Report the malaria status of this cell.
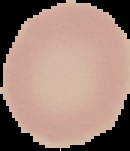

Uninfected.

Segmented cell region on a black background. Image is 130×151 pixels. From a thin blood film.